Point out leukocytes.
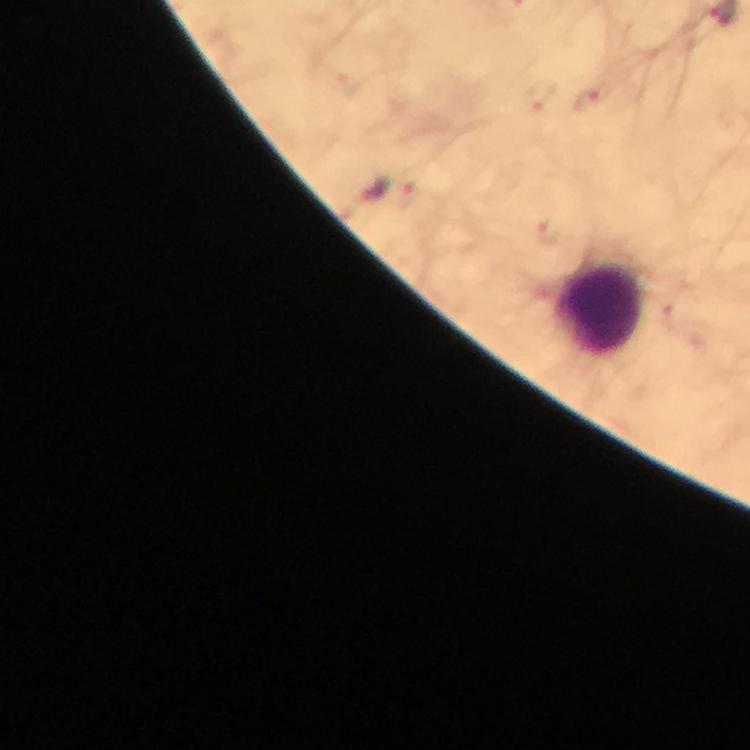
Approximate centers as {x, y} in pixels.
Leukocytes: {602, 312}.

Plasmodium parasite locations = approximate centers as {x, y} in pixels: {542, 98}, {590, 100}, {410, 197}, {547, 235}
image size = 750×750 pixels
cropped from = one field of view
capture = smartphone camera through the microscope
stain = Giemsa
preparation = thick smear
context = from a diagnostic examination for malaria
immersion oil = applied
magnification = 100x